Point out each Plasmodium parasite.
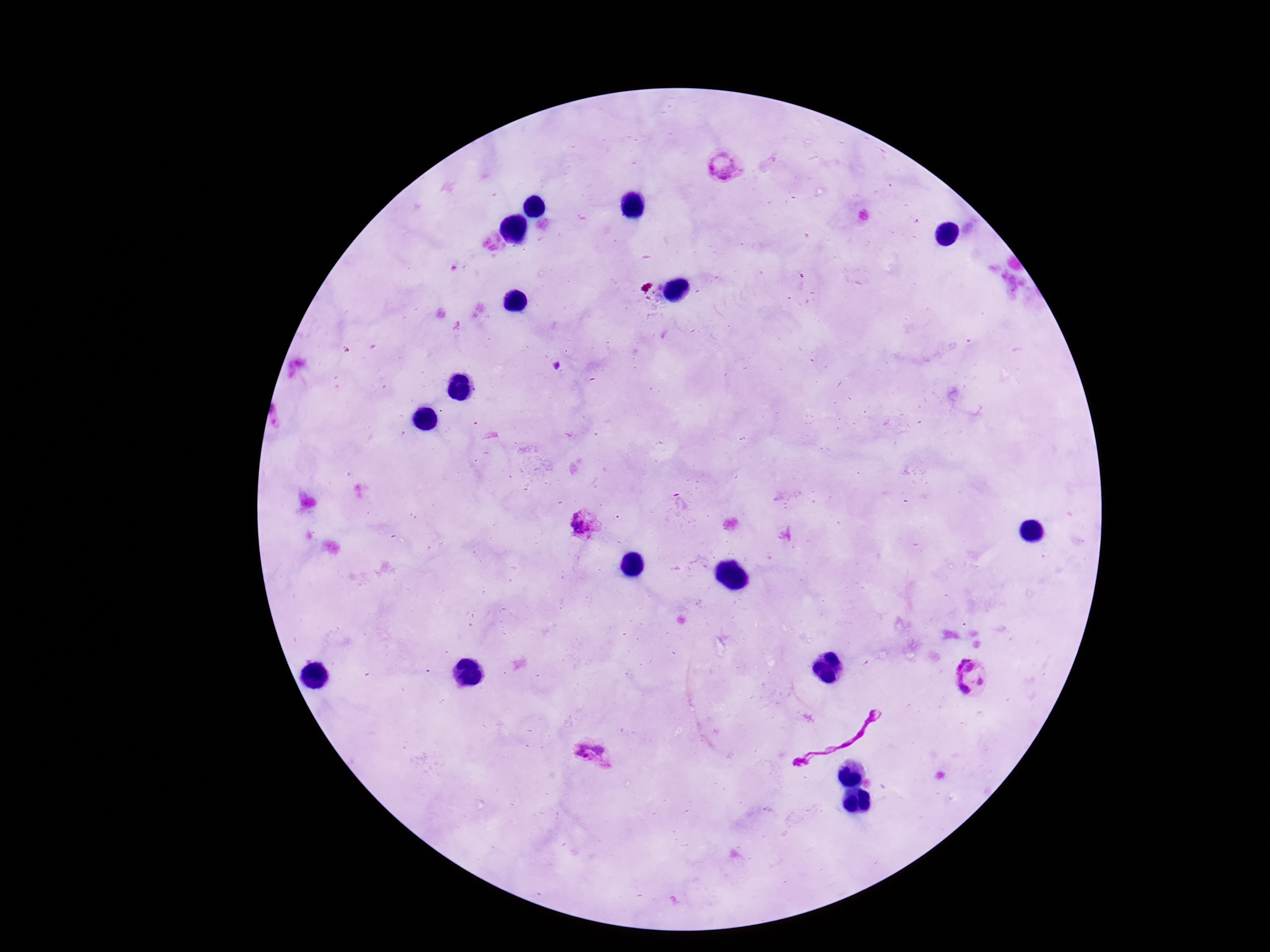
Approximate object centers, in pixels from the top-left corner.
Plasmodium parasites: (x=720, y=166), (x=584, y=524), (x=971, y=677), (x=593, y=754).

Summary:
  - Capture: smartphone camera through the microscope eyepiece
  - Field of view: one from this slide
  - Preparation: thick blood film
  - Magnification: 100x
  - Patient malaria status: infected
  - Stain: Giemsa
  - Image size: 1270×952 pixels